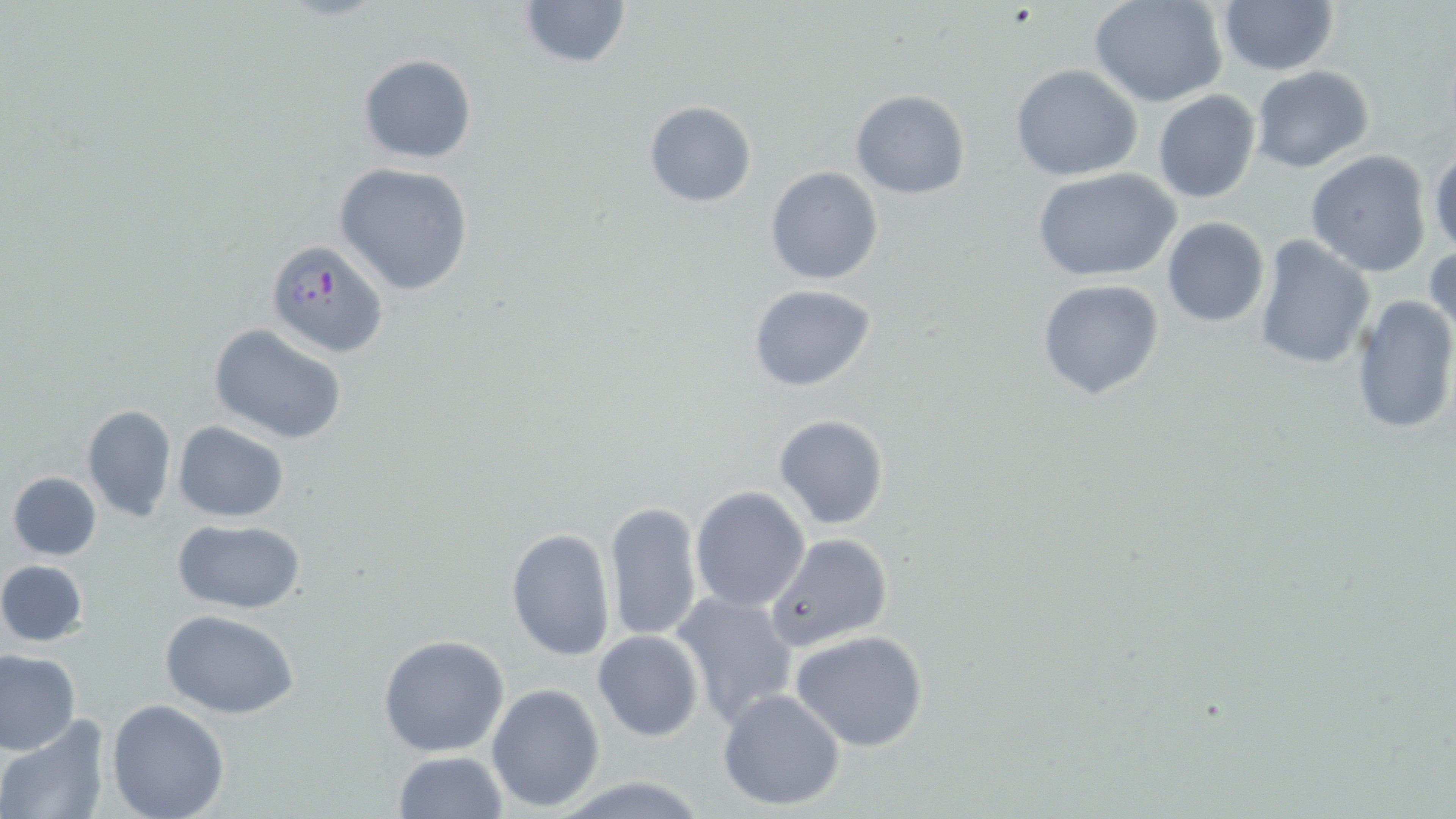 Approximate bounding boxes as named x1/y1/x2/y2 corners in pixels. Plasmodium falciparum-infected red blood cell locations: (x1=264, y1=237, x2=387, y2=355). Uninfected red blood cell locations: (x1=517, y1=0, x2=634, y2=72), (x1=1088, y1=0, x2=1227, y2=107), (x1=1216, y1=0, x2=1341, y2=76), (x1=357, y1=54, x2=478, y2=165), (x1=1009, y1=63, x2=1142, y2=181), (x1=1249, y1=65, x2=1374, y2=173), (x1=1153, y1=89, x2=1262, y2=204), (x1=850, y1=90, x2=969, y2=199), (x1=643, y1=100, x2=757, y2=208), (x1=1428, y1=149, x2=1456, y2=258), (x1=1305, y1=151, x2=1433, y2=277), (x1=333, y1=162, x2=475, y2=296), (x1=765, y1=165, x2=883, y2=285), (x1=1031, y1=168, x2=1182, y2=282), (x1=1161, y1=218, x2=1269, y2=327), (x1=1253, y1=235, x2=1375, y2=370), (x1=1427, y1=242, x2=1455, y2=347), (x1=1037, y1=279, x2=1166, y2=402), (x1=747, y1=284, x2=878, y2=392), (x1=1349, y1=293, x2=1456, y2=436), (x1=209, y1=323, x2=346, y2=446), (x1=80, y1=403, x2=177, y2=525), (x1=772, y1=413, x2=889, y2=531), (x1=172, y1=421, x2=289, y2=522), (x1=7, y1=471, x2=103, y2=560), (x1=691, y1=486, x2=811, y2=612), (x1=604, y1=500, x2=704, y2=643), (x1=174, y1=519, x2=306, y2=613), (x1=506, y1=528, x2=615, y2=661), (x1=764, y1=533, x2=893, y2=654), (x1=0, y1=559, x2=89, y2=648), (x1=672, y1=591, x2=799, y2=729), (x1=159, y1=609, x2=300, y2=717), (x1=592, y1=631, x2=705, y2=741), (x1=790, y1=631, x2=931, y2=752), (x1=377, y1=634, x2=510, y2=757), (x1=0, y1=650, x2=80, y2=754), (x1=486, y1=682, x2=604, y2=812), (x1=718, y1=688, x2=847, y2=811), (x1=106, y1=700, x2=230, y2=819), (x1=0, y1=719, x2=110, y2=819), (x1=392, y1=750, x2=508, y2=819), (x1=552, y1=776, x2=714, y2=817). Slide-level diagnosis: Plasmodium falciparum. Optical microscopy. One field of a larger specimen. May-Grünwald-Giemsa stain. Captured at 1000x magnification. Thin blood film. Image is 1456×819 pixels.